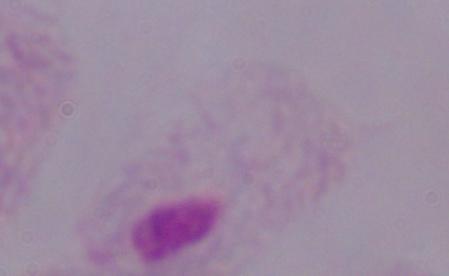

Summary:
  - Identification: trichomonad
  - Magnification: 1000x
  - Modality: micrograph